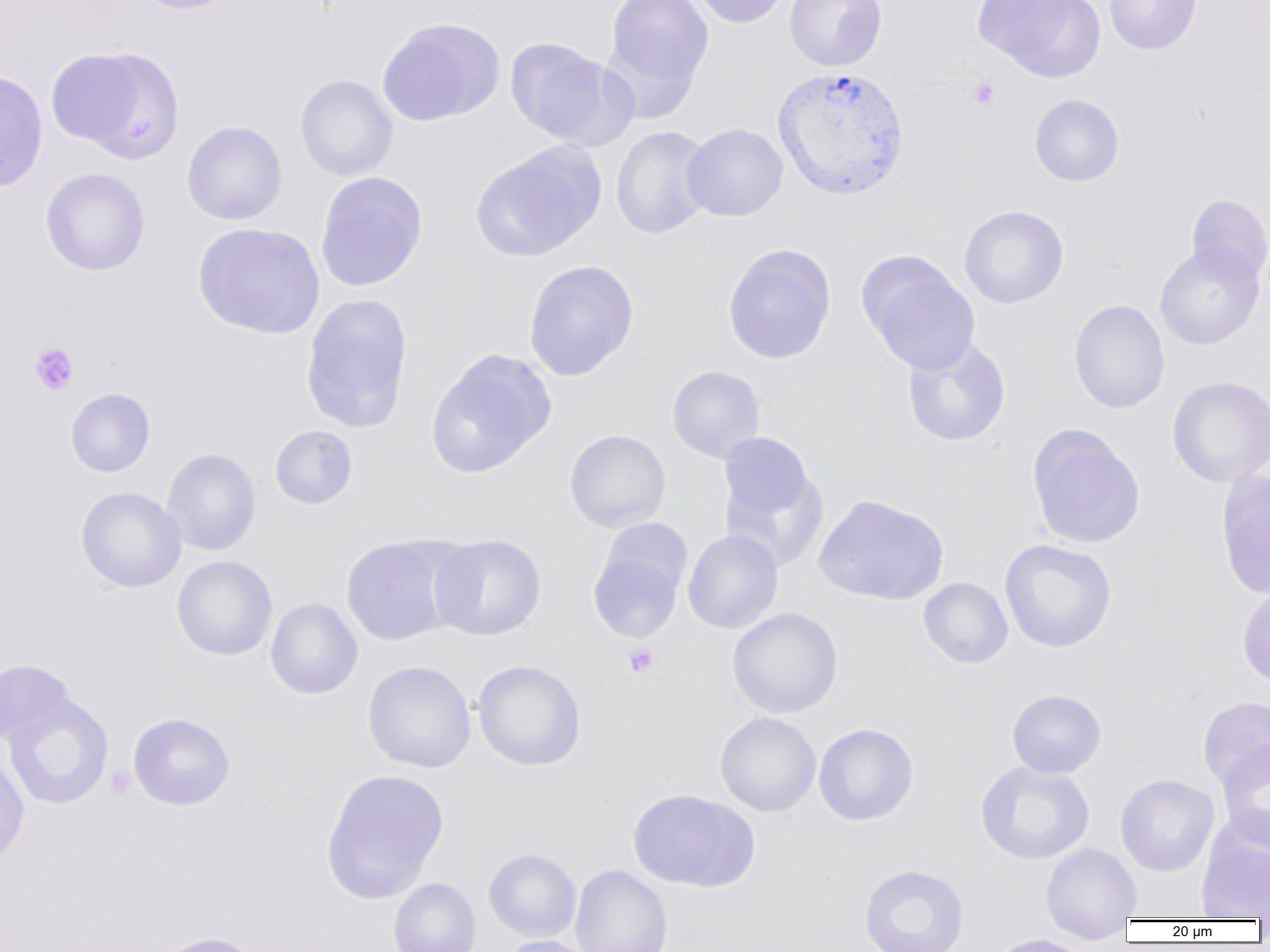

Summary:
  - Coordinate format: approximate bounding boxes as named x1/y1/x2/y2 corners in pixels
  - Plasmodium vivax-infected red blood cell locations: (x1=771, y1=65, x2=909, y2=201)
  - Uninfected red blood cell locations: (x1=130, y1=0, x2=245, y2=15), (x1=604, y1=0, x2=713, y2=94), (x1=690, y1=0, x2=792, y2=27), (x1=785, y1=0, x2=886, y2=71), (x1=974, y1=0, x2=1103, y2=81), (x1=1104, y1=0, x2=1202, y2=54), (x1=377, y1=18, x2=504, y2=126), (x1=505, y1=38, x2=632, y2=149), (x1=48, y1=45, x2=184, y2=162), (x1=0, y1=70, x2=48, y2=193), (x1=295, y1=74, x2=398, y2=181), (x1=1029, y1=94, x2=1124, y2=186), (x1=182, y1=121, x2=288, y2=225), (x1=681, y1=123, x2=788, y2=221), (x1=610, y1=126, x2=714, y2=239), (x1=472, y1=143, x2=605, y2=262), (x1=41, y1=167, x2=150, y2=275), (x1=315, y1=171, x2=427, y2=292), (x1=1186, y1=194, x2=1270, y2=285), (x1=959, y1=205, x2=1068, y2=308), (x1=192, y1=222, x2=324, y2=338), (x1=1155, y1=243, x2=1265, y2=350), (x1=722, y1=244, x2=836, y2=364), (x1=858, y1=253, x2=980, y2=375), (x1=524, y1=259, x2=638, y2=381), (x1=300, y1=293, x2=414, y2=434), (x1=1069, y1=300, x2=1169, y2=414), (x1=903, y1=336, x2=1011, y2=447), (x1=426, y1=349, x2=556, y2=478), (x1=667, y1=365, x2=765, y2=463), (x1=1166, y1=376, x2=1270, y2=487), (x1=66, y1=388, x2=155, y2=477), (x1=1026, y1=423, x2=1145, y2=549), (x1=270, y1=425, x2=358, y2=509), (x1=565, y1=429, x2=670, y2=532), (x1=716, y1=435, x2=828, y2=570), (x1=162, y1=448, x2=261, y2=555), (x1=1216, y1=470, x2=1270, y2=600), (x1=75, y1=486, x2=186, y2=592), (x1=813, y1=494, x2=949, y2=605), (x1=599, y1=519, x2=693, y2=600), (x1=683, y1=529, x2=783, y2=634), (x1=429, y1=534, x2=547, y2=640), (x1=340, y1=535, x2=457, y2=645), (x1=999, y1=539, x2=1117, y2=653), (x1=588, y1=550, x2=684, y2=642), (x1=172, y1=555, x2=277, y2=660), (x1=918, y1=577, x2=1013, y2=668), (x1=1237, y1=585, x2=1270, y2=691), (x1=265, y1=598, x2=363, y2=699), (x1=727, y1=607, x2=843, y2=718), (x1=472, y1=659, x2=586, y2=771), (x1=0, y1=660, x2=76, y2=747), (x1=362, y1=660, x2=476, y2=773), (x1=1007, y1=689, x2=1106, y2=778), (x1=3, y1=693, x2=113, y2=809), (x1=1198, y1=696, x2=1270, y2=790), (x1=715, y1=712, x2=821, y2=817), (x1=128, y1=713, x2=235, y2=810), (x1=813, y1=723, x2=919, y2=826), (x1=1216, y1=741, x2=1270, y2=850), (x1=0, y1=753, x2=29, y2=868), (x1=975, y1=760, x2=1095, y2=864), (x1=321, y1=768, x2=449, y2=902), (x1=1115, y1=774, x2=1219, y2=876), (x1=628, y1=788, x2=758, y2=892), (x1=1196, y1=814, x2=1270, y2=920), (x1=1040, y1=842, x2=1142, y2=939), (x1=484, y1=848, x2=581, y2=942), (x1=858, y1=863, x2=969, y2=952), (x1=570, y1=864, x2=672, y2=952), (x1=389, y1=877, x2=481, y2=952), (x1=151, y1=932, x2=265, y2=952), (x1=983, y1=934, x2=1097, y2=952), (x1=496, y1=935, x2=592, y2=952)
  - Platelet locations: (x1=968, y1=76, x2=1000, y2=110), (x1=29, y1=342, x2=79, y2=395), (x1=623, y1=643, x2=659, y2=677), (x1=105, y1=765, x2=136, y2=798)
  - Slide-level diagnosis: Plasmodium vivax
  - Preparation: thin blood smear
  - Modality: optical microscopy
  - Image size: 1270×952 pixels
  - Magnification: 1000x
  - Field of view: one of a larger specimen